Assess the morphology of the red blood cells.
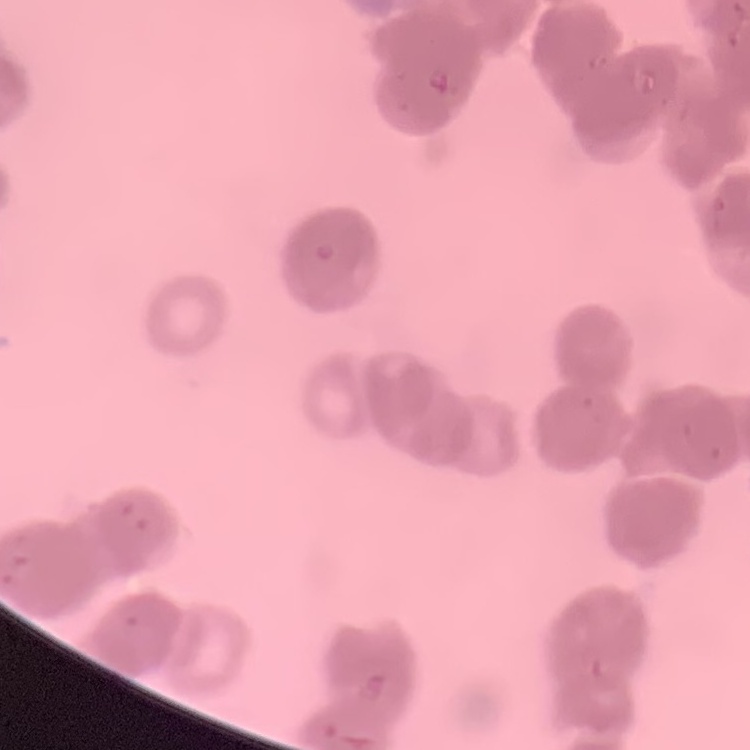
They show rouleaux formation.

Field's or Giemsa stain. Thin blood film. One tile cut from a larger photomicrograph.